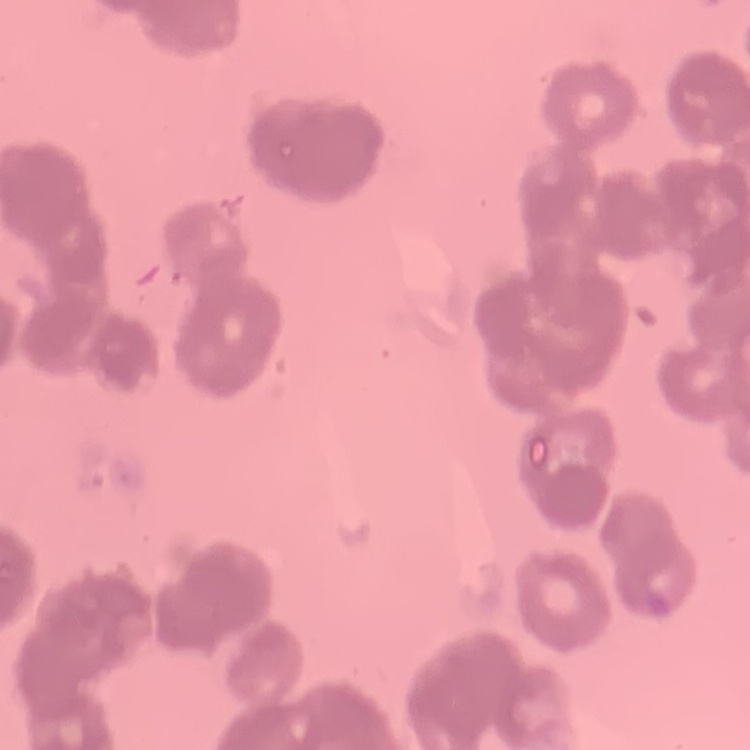
erythrocyte morphology = rouleaux formation
stain = Field's or Giemsa
image type = square crop of a larger photomicrograph
preparation = thin blood smear